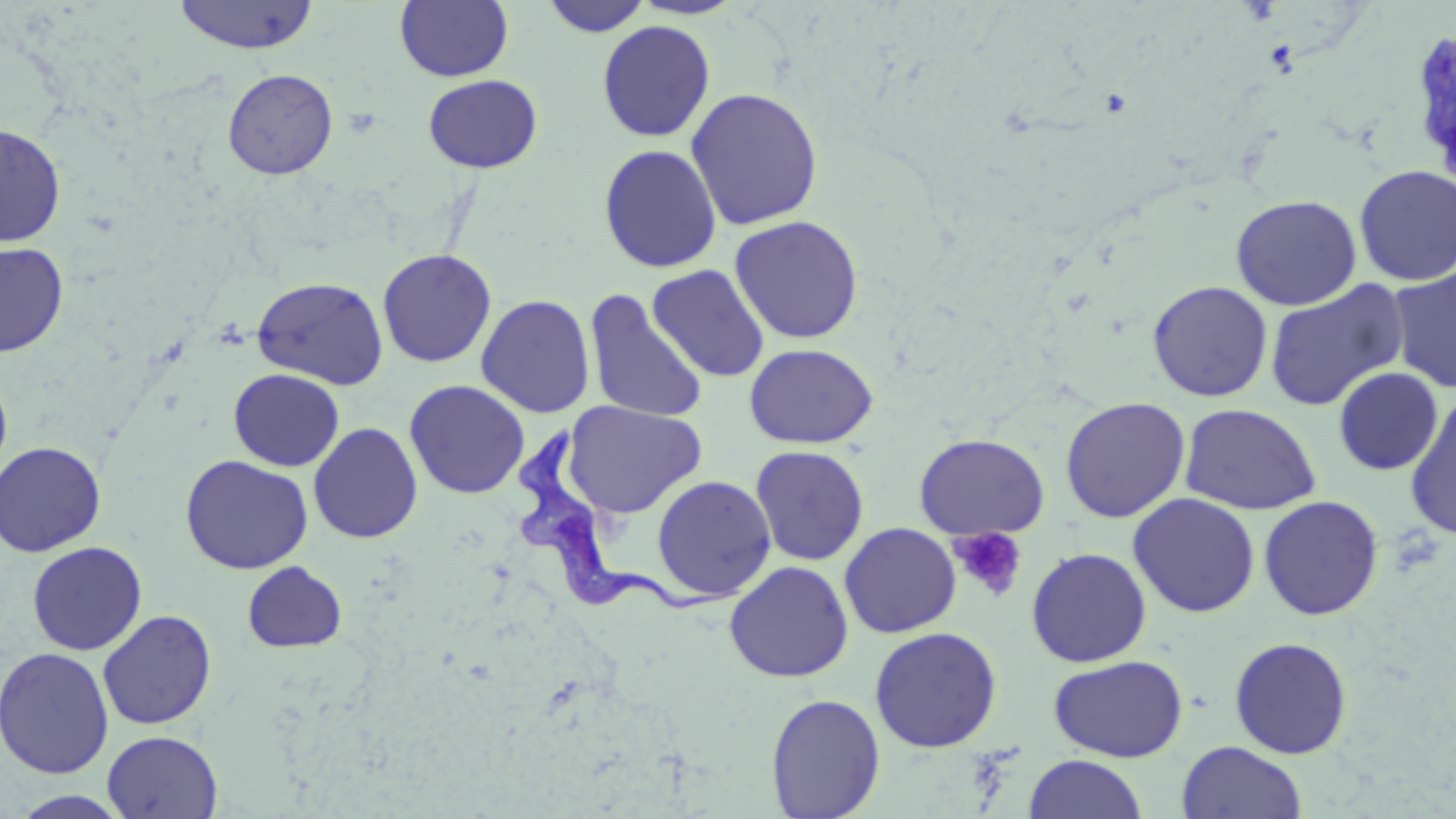

{
  "trypanosoma_brucei_locations": "approximate bounding boxes as (x1, y1, x2, y2) in pixels: (513, 423, 743, 613)",
  "slide_level_diagnosis": "Trypanosoma brucei",
  "uninfected_red_blood_cell_locations": "approximate bounding boxes as (x1, y1, x2, y2) in pixels: (172, 0, 319, 54), (395, 0, 513, 82), (539, 0, 653, 37), (596, 20, 716, 142), (1409, 25, 1455, 182), (222, 68, 338, 180), (423, 74, 543, 174), (686, 86, 824, 231), (0, 122, 66, 247), (598, 143, 722, 273), (1353, 165, 1456, 287), (1230, 194, 1362, 310), (728, 215, 865, 344), (0, 241, 69, 357), (377, 248, 497, 368), (647, 264, 770, 382), (1387, 266, 1456, 394), (252, 275, 389, 390), (1264, 279, 1409, 412), (1147, 280, 1273, 402), (584, 290, 707, 423), (476, 294, 595, 418), (744, 343, 878, 449), (0, 365, 13, 486), (1333, 367, 1443, 475), (228, 368, 344, 472), (404, 380, 530, 499), (1404, 393, 1456, 538), (1059, 396, 1191, 523), (562, 400, 707, 518), (1179, 403, 1322, 515), (308, 422, 423, 544), (913, 433, 1050, 539), (0, 441, 106, 557), (749, 444, 870, 566), (180, 454, 313, 574), (651, 474, 776, 601), (1128, 492, 1260, 618), (1258, 495, 1384, 620), (839, 522, 961, 638), (26, 541, 148, 655), (1025, 547, 1152, 667), (241, 561, 347, 653), (724, 561, 854, 683), (97, 609, 216, 730), (869, 626, 1003, 752), (1228, 636, 1353, 759), (0, 647, 115, 778), (1047, 654, 1189, 762), (765, 693, 885, 818), (102, 730, 223, 819), (1176, 741, 1307, 819), (1023, 755, 1149, 819), (8, 790, 134, 818)",
  "field_of_view": "one of a larger specimen",
  "preparation": "thin blood film",
  "image_size": "1456×819 pixels",
  "stain": "May-Grünwald-Giemsa",
  "magnification": "1000x",
  "modality": "light microscopy",
  "platelet_locations": "approximate bounding boxes as (x1, y1, x2, y2) in pixels: (950, 527, 1027, 603)"
}